Locate every blood parasite and identify its species.
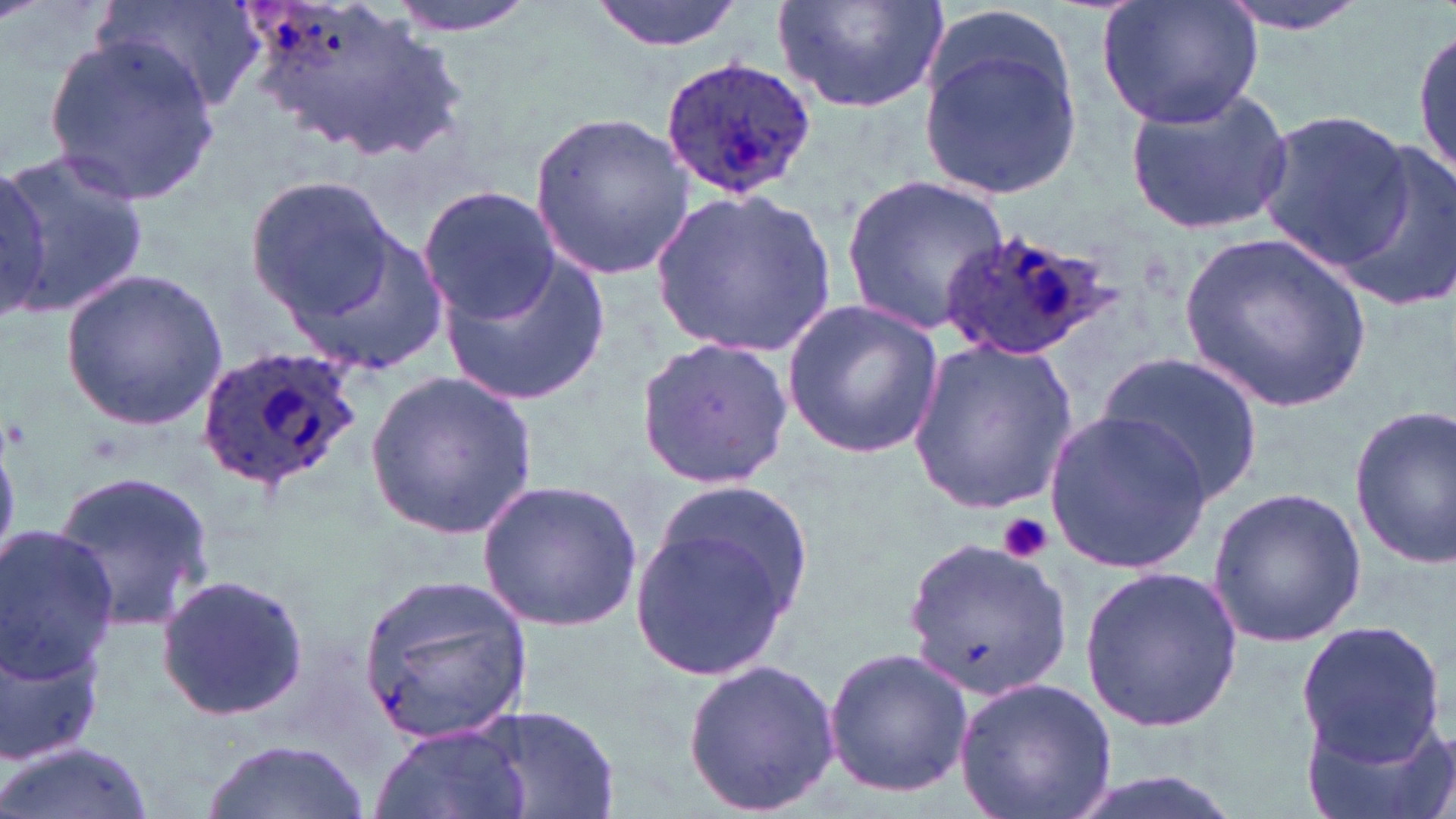

Approximate bounding boxes as (x1,y1)-(x2,y2) corner pairs in pixels.
Plasmodium ovale-infected red blood cells: (659,57)-(816,199), (939,225)-(1120,360), (195,344)-(363,494).
No Plasmodium falciparum, Plasmodium malariae, Plasmodium vivax, Babesia divergens, or Trypanosoma brucei observed.

Summary:
  - Uninfected red blood cell locations: (98,0)-(264,115), (234,0)-(452,155), (383,0)-(541,35), (590,0)-(746,53), (772,0)-(954,114), (1211,0)-(1375,36), (1097,1)-(1263,129), (925,5)-(1074,117), (1412,24)-(1454,186), (44,33)-(219,209), (920,39)-(1082,202), (1122,86)-(1297,234), (528,107)-(698,284), (1253,110)-(1411,267), (1328,136)-(1456,314), (0,141)-(150,320), (0,165)-(53,316), (244,173)-(399,323), (841,176)-(1009,334), (417,186)-(561,324), (650,186)-(836,357), (268,205)-(451,380), (1181,229)-(1372,413), (438,251)-(609,408), (59,269)-(229,430), (781,299)-(945,459), (634,336)-(794,490), (909,338)-(1078,513), (1095,352)-(1264,508), (366,369)-(537,538), (1349,403)-(1455,571), (1043,408)-(1213,575), (53,469)-(213,630), (476,476)-(643,633), (1208,486)-(1365,645), (630,495)-(815,679), (0,526)-(124,680), (905,538)-(1071,703), (1079,564)-(1243,733), (362,573)-(535,745), (156,574)-(308,723), (1,605)-(115,772), (1294,621)-(1448,765), (823,646)-(975,798), (682,658)-(844,817), (953,677)-(1119,819), (465,706)-(623,819), (1295,708)-(1455,819), (368,721)-(533,819), (199,740)-(374,819), (0,741)-(157,819)
  - Platelet locations: (999,513)-(1053,563)
  - Slide-level diagnosis: Plasmodium ovale
  - Magnification: 1000x
  - Preparation: thin blood film
  - Image size: 1456×819 pixels
  - Field of view: one of a larger specimen
  - Stain: May-Grünwald-Giemsa
  - Modality: optical microscopy